Assess the morphology of the red blood cells.
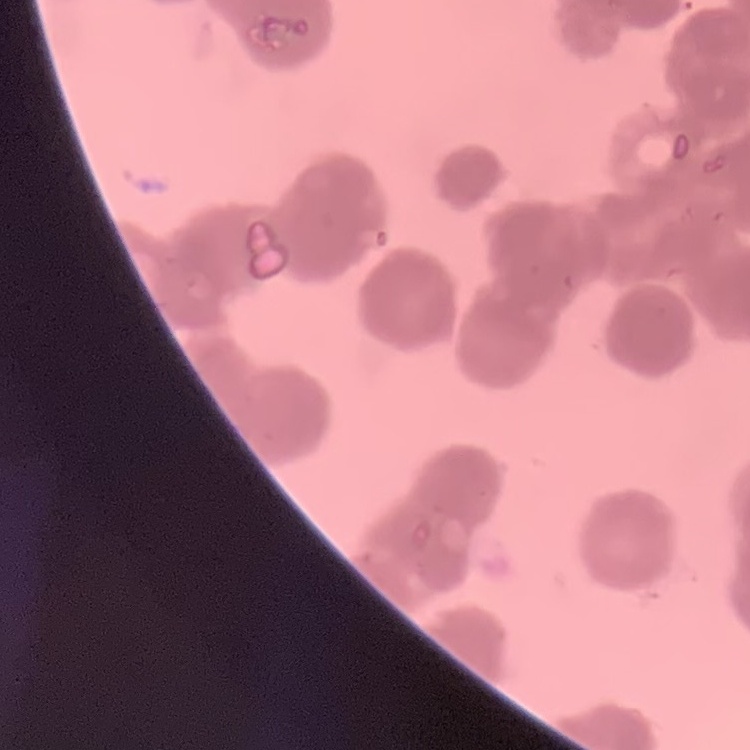

Rouleaux formation.

Stained with either Field's or Giemsa. Thin blood film. Square crop of a larger photomicrograph.